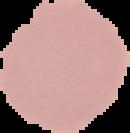

Cell region segmented out of the field of view; the surrounding area is masked to black. Result: no Plasmodium parasites seen. Image is 130×133 pixels. From a thin blood smear.